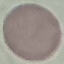

Summary:
  - Malaria status: uninfected
  - Image type: automatically extracted cell patch, resized to 64 × 64 pixels
  - Preparation: thin smear
  - Stain: Giemsa
  - Capture: smartphone through the microscope eyepiece